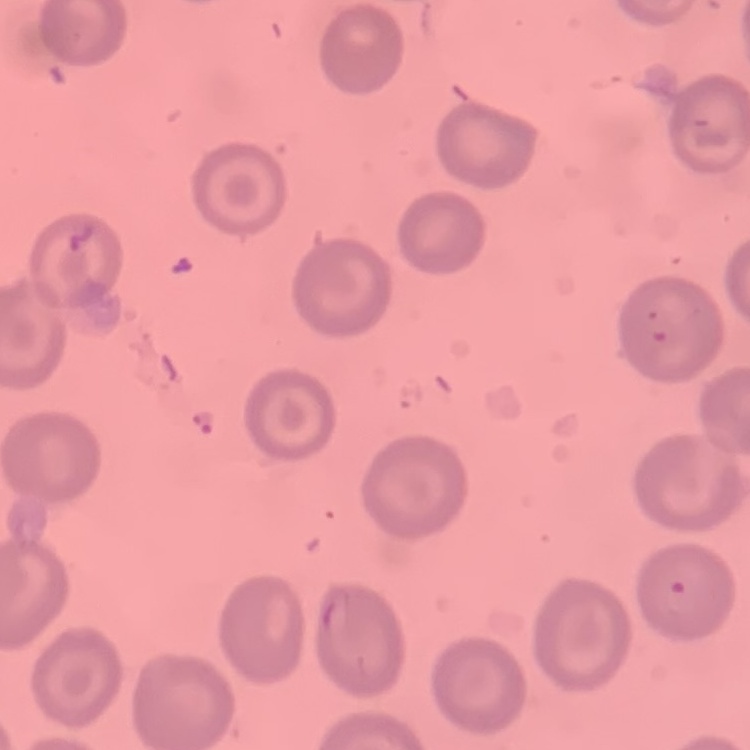

{
  "erythrocyte_morphology": "no rouleaux formation",
  "preparation": "thin peripheral smear",
  "image_type": "one tile cut from a larger photomicrograph",
  "stain": "Field's or Giemsa"
}